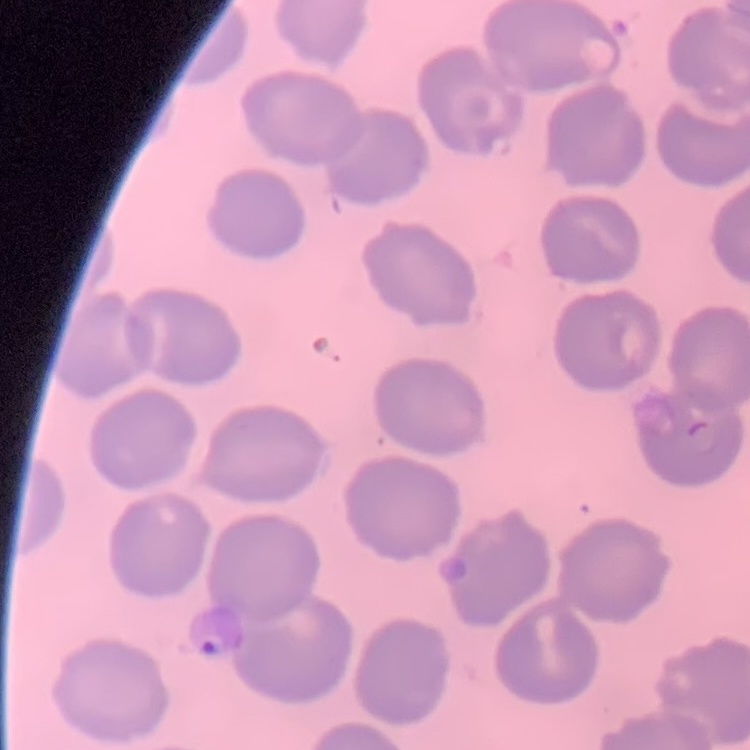

red_blood_cell_morphology: no rouleaux formation
stain: Field's or Giemsa
image_type: one tile cut from a larger photomicrograph
preparation: thin blood film